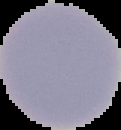 Malaria status: uninfected. Image is 121×130 pixels. Cell region segmented out of the field of view; the surrounding area is masked to black. From a thin blood film.